Assess for Plasmodium parasites.
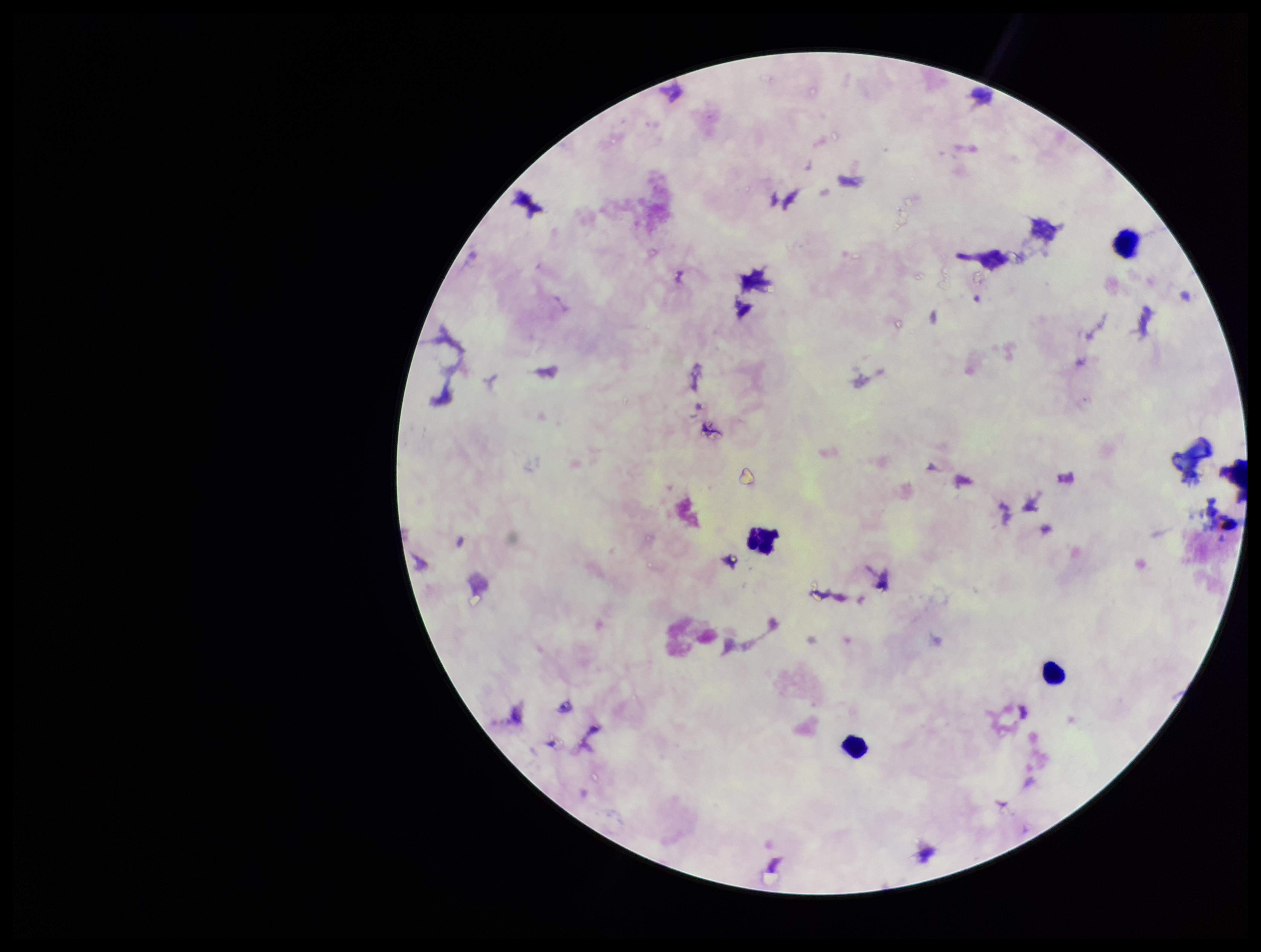
None identified.

{
  "stain": "Giemsa",
  "patient_malaria_status": "negative",
  "leukocyte_count": 4,
  "parasite_count": 0,
  "image_size": "1261×952 pixels",
  "field_of_view": "one from this slide",
  "preparation": "thick",
  "capture": "smartphone photograph through the microscope eyepiece"
}